State which parasite is depicted.
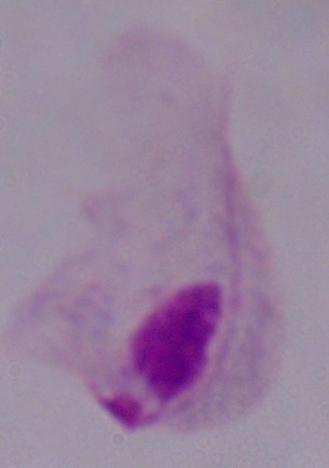
A trichomonad.

magnification = 1000x
modality = photomicrograph